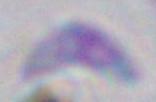

Toxoplasma gondii is shown. Captured at 1000x magnification. Photomicrograph.